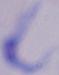
modality = photomicrograph
identification = trypanosome
magnification = 1000x